Classify this cell by malaria status.
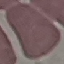
Uninfected.

capture = smartphone through the microscope eyepiece
preparation = thin blood film
stain = Giemsa
image type = cell patch, automatically extracted from a larger field of view and resized to 64 × 64 pixels